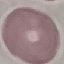
Summary:
  - Result: no malaria parasites detected
  - Stain: Giemsa
  - Capture: smartphone camera at the microscope eyepiece
  - Image type: cell patch, automatically extracted from a larger field of view and resized to 64 × 64 pixels
  - Preparation: thin smear